Point out each Plasmodium parasite and each leukocyte.
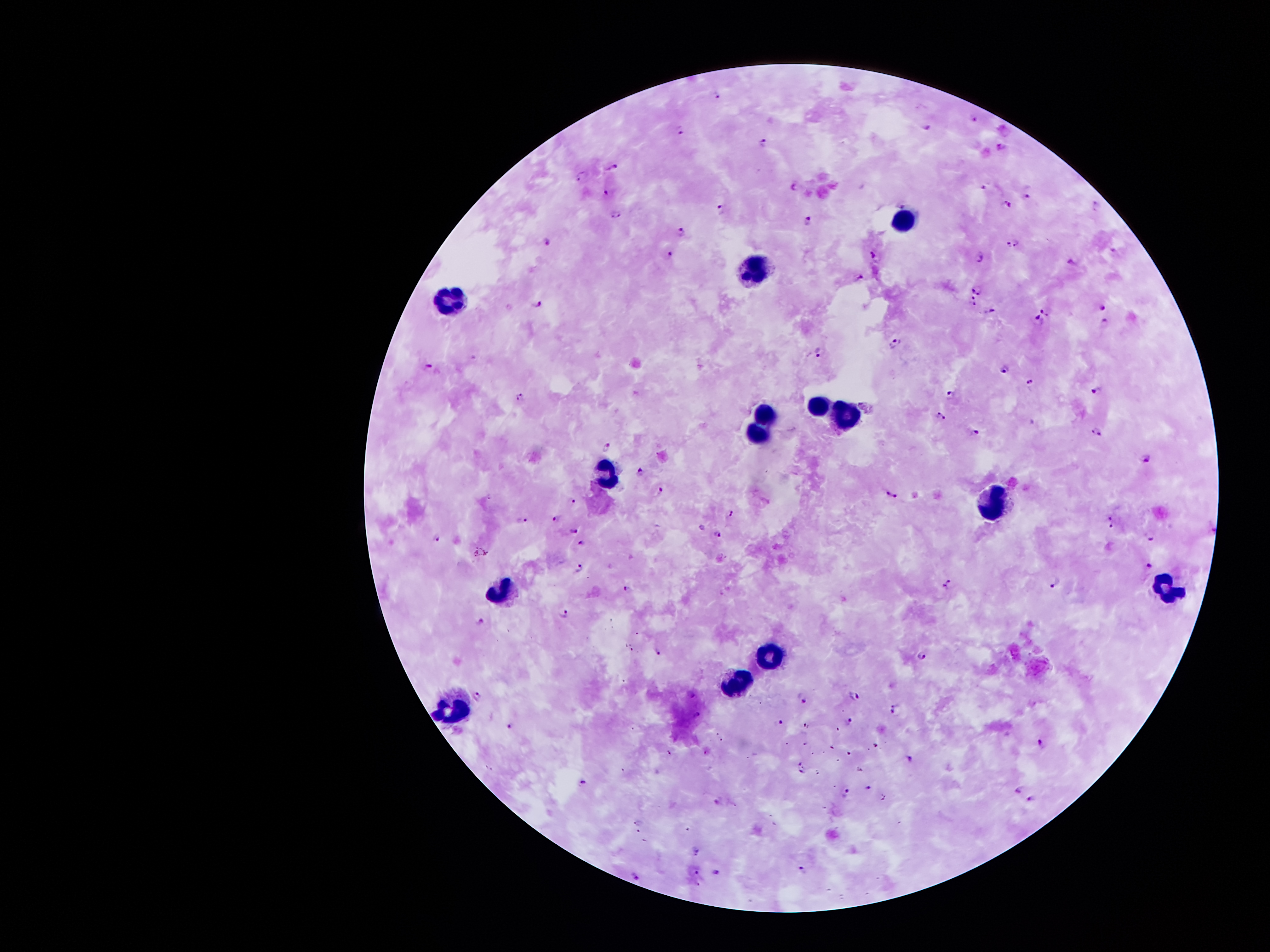
Approximate centers as {x, y} in pixels.
Plasmodium parasites: {718, 94}, {974, 118}, {925, 128}, {679, 131}, {764, 142}, {1000, 146}, {612, 167}, {581, 175}, {795, 186}, {983, 186}, {605, 192}, {1030, 192}, {1008, 204}, {1095, 207}, {720, 208}, {616, 215}, {808, 219}, {680, 232}, {1008, 243}, {548, 244}, {1017, 245}, {1115, 253}, {669, 254}, {876, 257}, {980, 257}, {1073, 263}, {860, 279}, {977, 288}, {974, 301}, {539, 305}, {1101, 306}, {990, 311}, {1044, 311}, {1038, 320}, {1105, 321}, {894, 344}, {819, 352}, {429, 366}, {1005, 370}, {1031, 381}, {1098, 389}, {951, 392}, {519, 396}, {940, 416}, {973, 431}, {1095, 433}, {606, 447}, {1147, 458}, {640, 470}, {659, 490}, {890, 493}, {573, 499}, {729, 515}, {557, 518}, {522, 521}, {1111, 522}, {702, 526}, {574, 529}, {718, 534}, {437, 536}, {1150, 537}, {582, 541}, {1150, 566}, {580, 568}, {948, 584}, {1057, 585}, {628, 589}, {564, 613}, {481, 622}, {656, 652}, {923, 657}, {478, 694}, {855, 696}, {803, 697}, {895, 708}, {849, 721}, {777, 722}, {510, 725}, {1042, 742}, {850, 752}, {910, 759}, {802, 767}, {583, 783}, {868, 789}, {1020, 789}, {847, 793}, {1032, 799}, {716, 801}, {698, 850}, {804, 869}, {696, 871}, {718, 872}, {636, 876}.
Leukocytes: {907, 216}, {756, 268}, {455, 299}, {820, 404}, {852, 409}, {767, 411}, {755, 436}, {608, 472}, {989, 509}, {500, 590}, {1166, 590}, {771, 644}, {737, 675}, {451, 712}.

Summary:
  - Stain: Giemsa
  - Image size: 1270×952 pixels
  - Magnification: 100x
  - Patient malaria status: infected with Plasmodium falciparum
  - Preparation: thick blood smear
  - Field of view: one from this slide
  - Capture: smartphone through the microscope eyepiece